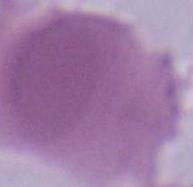

magnification = 1000x
modality = micrograph
identification = erythrocyte